State which parasite is depicted.
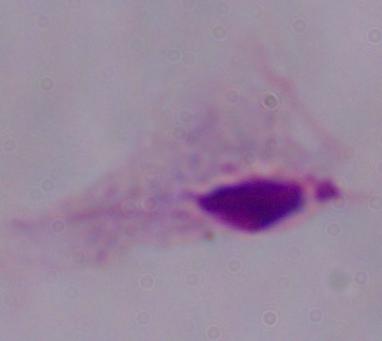
A trichomonad.

Captured at 1000x magnification. Micrograph.